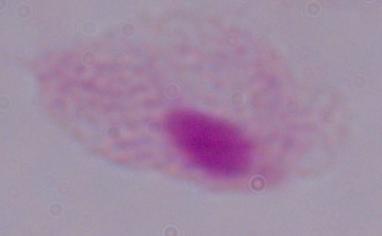
Summary:
  - Identification: trichomonad
  - Magnification: 1000x
  - Modality: photomicrograph